Locate every blood parasite and identify its species.
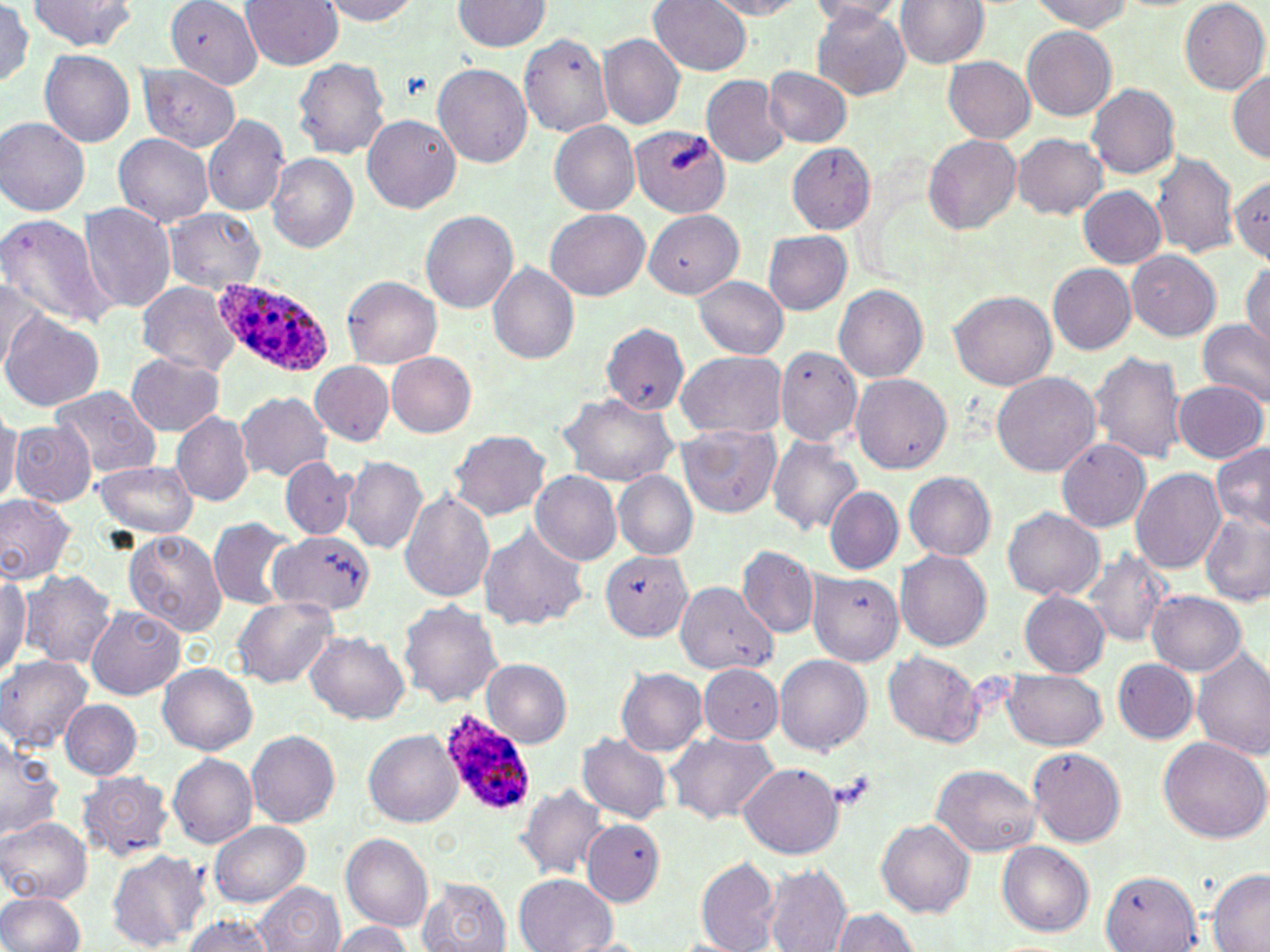
Approximate bounding boxes as named x1/y1/x2/y2 corners in pixels.
Plasmodium ovale-infected red blood cells: (x1=212, y1=279, x2=336, y2=377), (x1=436, y1=710, x2=534, y2=820).
No Plasmodium falciparum, Plasmodium malariae, Plasmodium vivax, Babesia divergens, or Trypanosoma brucei observed.

Uninfected red blood cell locations: (x1=28, y1=0, x2=137, y2=52), (x1=168, y1=0, x2=263, y2=91), (x1=240, y1=0, x2=344, y2=70), (x1=319, y1=0, x2=423, y2=24), (x1=706, y1=0, x2=809, y2=18), (x1=0, y1=1, x2=37, y2=88), (x1=452, y1=1, x2=549, y2=51), (x1=648, y1=1, x2=753, y2=75), (x1=805, y1=1, x2=908, y2=23), (x1=1028, y1=1, x2=1136, y2=32), (x1=1180, y1=1, x2=1269, y2=92), (x1=895, y1=3, x2=988, y2=69), (x1=810, y1=5, x2=912, y2=100), (x1=1022, y1=26, x2=1117, y2=120), (x1=519, y1=32, x2=614, y2=137), (x1=598, y1=33, x2=684, y2=130), (x1=41, y1=50, x2=135, y2=147), (x1=292, y1=57, x2=390, y2=158), (x1=943, y1=57, x2=1036, y2=144), (x1=432, y1=63, x2=531, y2=168), (x1=138, y1=64, x2=242, y2=151), (x1=764, y1=66, x2=852, y2=147), (x1=1228, y1=67, x2=1270, y2=164), (x1=701, y1=75, x2=789, y2=167), (x1=1087, y1=83, x2=1180, y2=179), (x1=202, y1=114, x2=291, y2=216), (x1=362, y1=115, x2=460, y2=213), (x1=1, y1=118, x2=91, y2=216), (x1=549, y1=121, x2=640, y2=214), (x1=630, y1=125, x2=729, y2=215), (x1=113, y1=133, x2=214, y2=228), (x1=1012, y1=133, x2=1108, y2=218), (x1=923, y1=135, x2=1023, y2=233), (x1=784, y1=143, x2=875, y2=233), (x1=1151, y1=152, x2=1240, y2=259), (x1=265, y1=153, x2=358, y2=252), (x1=1230, y1=173, x2=1270, y2=263), (x1=1078, y1=186, x2=1166, y2=268), (x1=79, y1=203, x2=176, y2=312), (x1=545, y1=208, x2=649, y2=300), (x1=163, y1=209, x2=265, y2=293), (x1=642, y1=209, x2=744, y2=298), (x1=421, y1=210, x2=518, y2=311), (x1=0, y1=212, x2=110, y2=327), (x1=763, y1=229, x2=852, y2=314), (x1=1125, y1=249, x2=1221, y2=341), (x1=1241, y1=261, x2=1270, y2=353), (x1=488, y1=263, x2=579, y2=363), (x1=1048, y1=263, x2=1137, y2=354), (x1=342, y1=276, x2=441, y2=368), (x1=691, y1=276, x2=789, y2=358), (x1=1, y1=279, x2=48, y2=374), (x1=136, y1=280, x2=243, y2=374), (x1=834, y1=283, x2=927, y2=384), (x1=948, y1=290, x2=1057, y2=392), (x1=1, y1=311, x2=103, y2=412), (x1=1198, y1=320, x2=1270, y2=405), (x1=600, y1=322, x2=688, y2=414), (x1=774, y1=346, x2=862, y2=445), (x1=675, y1=349, x2=788, y2=440), (x1=1089, y1=351, x2=1188, y2=464), (x1=387, y1=352, x2=476, y2=437), (x1=126, y1=353, x2=225, y2=436), (x1=311, y1=360, x2=394, y2=447), (x1=991, y1=371, x2=1100, y2=476), (x1=851, y1=373, x2=951, y2=471), (x1=1172, y1=379, x2=1267, y2=463), (x1=51, y1=385, x2=162, y2=480), (x1=236, y1=391, x2=332, y2=482), (x1=559, y1=394, x2=677, y2=486), (x1=0, y1=406, x2=20, y2=508), (x1=171, y1=409, x2=254, y2=506), (x1=10, y1=419, x2=96, y2=506), (x1=676, y1=423, x2=781, y2=517), (x1=448, y1=430, x2=551, y2=522), (x1=767, y1=437, x2=862, y2=535), (x1=1057, y1=438, x2=1150, y2=532), (x1=1210, y1=441, x2=1270, y2=529), (x1=341, y1=454, x2=429, y2=554), (x1=280, y1=457, x2=356, y2=543), (x1=91, y1=459, x2=200, y2=539), (x1=1131, y1=467, x2=1226, y2=573), (x1=530, y1=470, x2=623, y2=566), (x1=613, y1=471, x2=698, y2=559), (x1=904, y1=471, x2=996, y2=560), (x1=824, y1=487, x2=903, y2=576), (x1=398, y1=490, x2=495, y2=604), (x1=0, y1=494, x2=75, y2=583), (x1=1002, y1=507, x2=1105, y2=601), (x1=1201, y1=513, x2=1269, y2=606), (x1=209, y1=518, x2=296, y2=610), (x1=477, y1=524, x2=589, y2=632), (x1=123, y1=530, x2=227, y2=635), (x1=272, y1=531, x2=376, y2=617), (x1=735, y1=545, x2=820, y2=638), (x1=894, y1=548, x2=992, y2=650), (x1=1085, y1=548, x2=1169, y2=645), (x1=599, y1=550, x2=693, y2=641), (x1=0, y1=570, x2=30, y2=677), (x1=21, y1=570, x2=117, y2=668), (x1=808, y1=570, x2=902, y2=662), (x1=678, y1=584, x2=776, y2=704), (x1=1019, y1=591, x2=1109, y2=678), (x1=1146, y1=591, x2=1246, y2=675), (x1=232, y1=596, x2=339, y2=689), (x1=397, y1=600, x2=506, y2=708), (x1=85, y1=604, x2=186, y2=700), (x1=305, y1=632, x2=409, y2=723), (x1=1192, y1=649, x2=1270, y2=761), (x1=882, y1=651, x2=984, y2=747), (x1=773, y1=654, x2=872, y2=753), (x1=0, y1=655, x2=94, y2=752), (x1=483, y1=659, x2=571, y2=746), (x1=1113, y1=659, x2=1198, y2=744), (x1=157, y1=663, x2=257, y2=754), (x1=697, y1=663, x2=784, y2=744), (x1=616, y1=666, x2=708, y2=755), (x1=1003, y1=669, x2=1107, y2=749), (x1=60, y1=698, x2=142, y2=780), (x1=246, y1=729, x2=339, y2=828), (x1=363, y1=730, x2=463, y2=827), (x1=664, y1=731, x2=780, y2=825), (x1=0, y1=733, x2=64, y2=841), (x1=577, y1=733, x2=672, y2=823), (x1=1158, y1=736, x2=1270, y2=841), (x1=1027, y1=746, x2=1126, y2=847), (x1=168, y1=753, x2=258, y2=848), (x1=738, y1=761, x2=845, y2=858), (x1=931, y1=763, x2=1041, y2=856), (x1=76, y1=770, x2=174, y2=863), (x1=516, y1=785, x2=609, y2=880), (x1=0, y1=817, x2=92, y2=903), (x1=876, y1=819, x2=974, y2=917), (x1=581, y1=820, x2=665, y2=909), (x1=209, y1=821, x2=310, y2=907), (x1=340, y1=832, x2=433, y2=931), (x1=997, y1=841, x2=1093, y2=936), (x1=104, y1=849, x2=210, y2=951), (x1=695, y1=855, x2=780, y2=951), (x1=764, y1=866, x2=851, y2=951), (x1=1205, y1=869, x2=1270, y2=952), (x1=1100, y1=870, x2=1202, y2=952), (x1=516, y1=875, x2=615, y2=951), (x1=418, y1=879, x2=513, y2=952), (x1=254, y1=882, x2=342, y2=952), (x1=0, y1=891, x2=86, y2=951), (x1=828, y1=908, x2=919, y2=952), (x1=181, y1=913, x2=275, y2=951), (x1=326, y1=921, x2=414, y2=952). Slide-level diagnosis: Plasmodium ovale. Light microscopy. May-Grünwald-Giemsa stain. Captured at 1000x magnification. Thin blood film. One field of a larger specimen. Image is 1270×952 pixels.